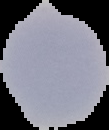

Summary:
  - Malaria status: uninfected
  - Image type: segmented cell region on a black background
  - Image size: 109×130 pixels
  - Preparation: thin blood film